Point out every malaria parasite and every leukocyte.
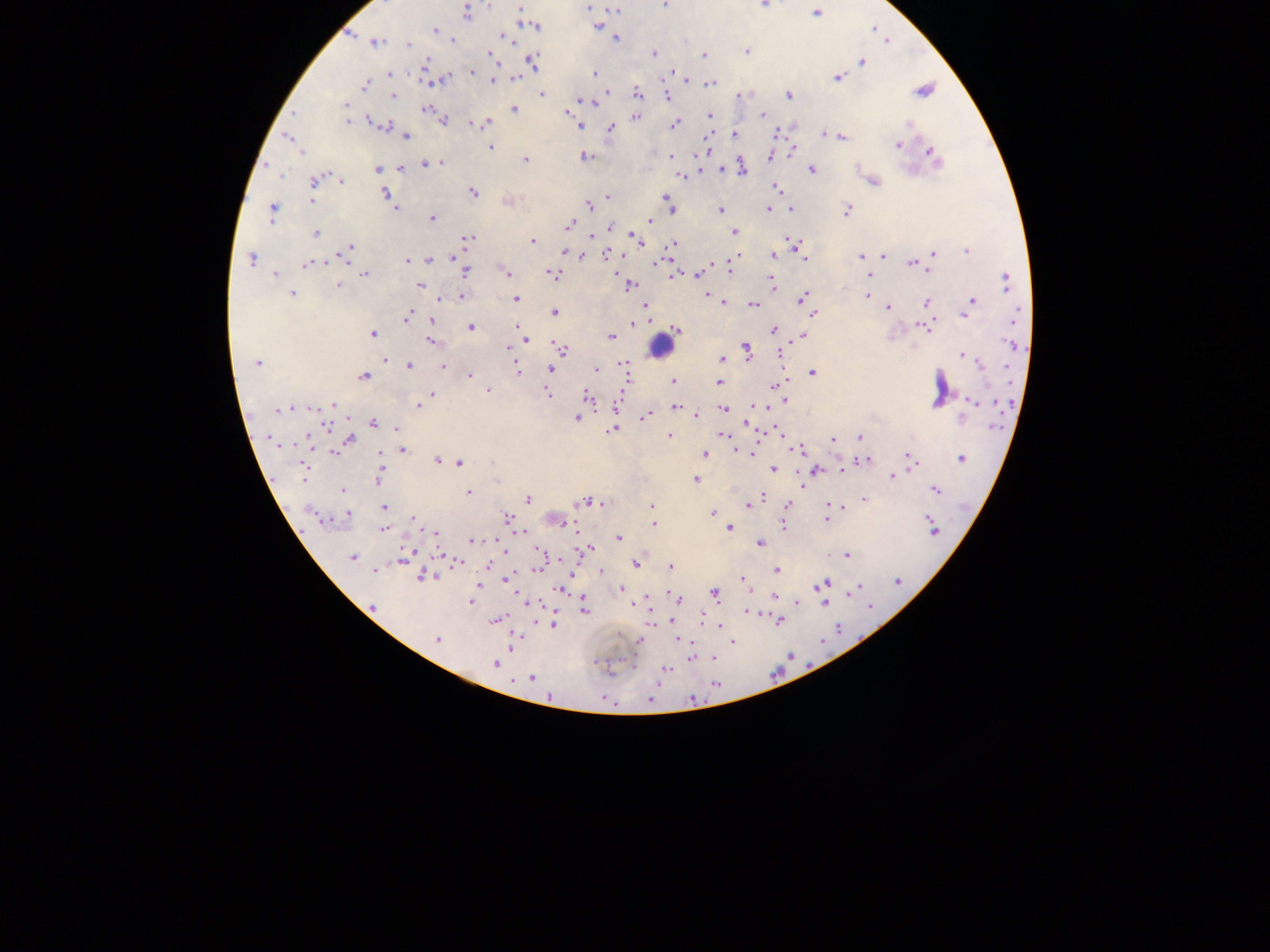
Approximate centers as (x, y) in pixels.
Malaria parasites: (489, 4), (665, 5), (764, 5), (520, 8), (589, 8), (616, 10), (467, 13), (816, 14), (536, 26), (599, 27), (435, 31), (503, 36), (616, 39), (452, 40), (376, 42), (408, 44), (747, 51), (655, 53), (703, 55), (491, 57), (532, 61), (862, 62), (426, 64), (471, 72), (595, 72), (391, 74), (515, 78), (685, 78), (837, 78), (494, 80), (434, 82), (711, 83), (365, 85), (922, 91), (607, 92), (542, 94), (638, 94), (789, 95), (393, 96), (667, 97), (581, 100), (345, 105), (426, 110), (514, 110), (567, 112), (293, 114), (710, 115), (763, 115), (635, 117), (443, 121), (347, 122), (486, 124), (383, 125), (674, 125), (909, 125), (579, 126), (610, 128), (735, 133), (825, 134), (841, 136), (406, 137), (287, 138), (898, 144), (490, 147), (792, 150), (301, 152), (585, 156), (672, 156), (771, 156), (934, 156), (525, 160), (441, 163), (425, 164), (401, 168), (378, 169), (721, 169), (743, 169), (811, 170), (280, 175), (682, 176), (315, 180), (341, 180), (874, 182), (776, 188), (474, 193), (386, 194), (607, 196), (665, 197), (311, 200), (589, 206), (670, 208), (768, 208), (395, 209), (721, 209), (791, 209), (847, 210), (272, 212), (432, 219), (649, 221), (569, 225), (609, 228), (734, 232), (315, 233), (634, 237), (469, 238), (637, 239), (533, 241), (790, 242), (795, 244), (672, 245), (350, 247), (346, 251), (966, 251), (564, 252), (573, 254), (608, 254), (803, 254), (933, 254), (773, 255), (884, 255), (581, 256), (861, 256), (455, 257), (252, 259), (805, 259), (429, 260), (407, 261), (411, 261), (307, 264), (911, 264), (927, 270), (464, 271), (506, 271), (731, 271), (868, 271), (552, 273), (365, 274), (698, 274), (674, 275), (869, 275), (275, 276), (1006, 281), (771, 282), (338, 286), (420, 286), (630, 286), (292, 294), (461, 296), (708, 296), (867, 296), (802, 298), (443, 299), (516, 299), (870, 299), (723, 302), (927, 302), (971, 302), (754, 304), (888, 307), (967, 308), (554, 312), (1017, 313), (813, 314), (407, 316), (432, 320), (634, 324), (471, 327), (923, 327), (519, 329), (677, 330), (775, 330), (373, 334), (803, 335), (611, 337), (526, 340), (430, 341), (1011, 345), (509, 348), (747, 348), (560, 349), (781, 354), (962, 355), (722, 359), (386, 362), (257, 363), (978, 363), (409, 365), (625, 366), (442, 367), (551, 368), (596, 369), (516, 370), (812, 373), (469, 375), (363, 377), (673, 381), (718, 383), (775, 385), (488, 390), (548, 393), (432, 394), (586, 395), (783, 400), (972, 402), (334, 404), (418, 405), (616, 406), (676, 407), (313, 409), (723, 409), (290, 410), (278, 411), (646, 415), (697, 415), (578, 418), (373, 422), (747, 423), (327, 426), (397, 429), (612, 430), (723, 435), (669, 436), (859, 437), (350, 439), (270, 440), (833, 440), (799, 449), (402, 451), (334, 452), (745, 452), (705, 454), (380, 455), (961, 459), (912, 460), (437, 461), (864, 461), (460, 462), (774, 469), (304, 471), (816, 471), (893, 476), (379, 477), (695, 479), (935, 489), (342, 490), (468, 493), (763, 497), (527, 499), (864, 499), (584, 501), (595, 502), (601, 503), (748, 504), (787, 505), (653, 506), (384, 507), (834, 507), (347, 514), (712, 514), (316, 517), (508, 518), (413, 519), (827, 520), (654, 524), (783, 524), (729, 528), (931, 528), (383, 530), (435, 532), (619, 538), (472, 540), (760, 544), (588, 548), (504, 551), (847, 555), (352, 557), (403, 560), (456, 562), (636, 564), (489, 566), (670, 568), (776, 570), (374, 571), (601, 571), (422, 576), (506, 580), (897, 581), (744, 582), (823, 584), (479, 585), (560, 589), (622, 589), (856, 589), (715, 594), (677, 598), (775, 598), (470, 602), (798, 602), (824, 603), (528, 604), (373, 606), (585, 610), (747, 612), (497, 620), (779, 622), (552, 624), (720, 627), (437, 639), (639, 640), (681, 641), (732, 642), (512, 647), (713, 658), (495, 664), (665, 670), (531, 678), (650, 700).
Leukocytes: (658, 345).

capture = mobile-phone photograph through a microscope
preparation = thick blood smear
image size = 1270×952 pixels
country = Ghana
field of view = single